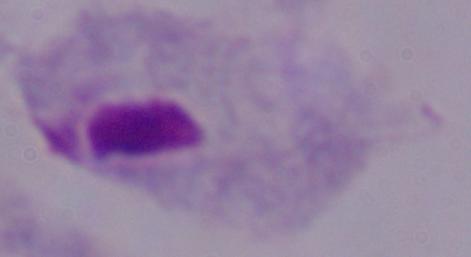

A trichomonad is seen. Captured at 1000x magnification. Micrograph.